Outline platelets.
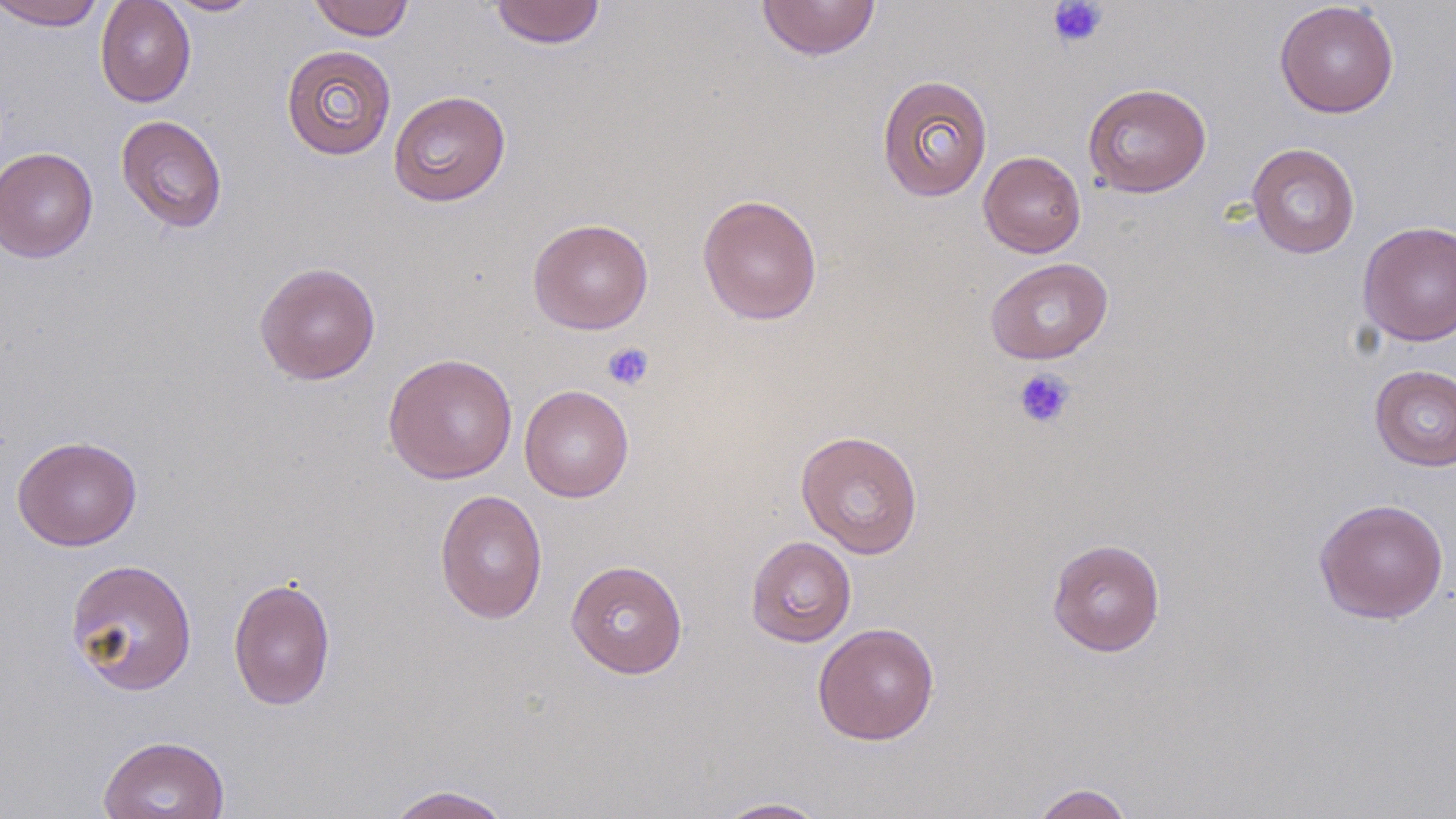
Approximate bounding boxes as named x1/y1/x2/y2 corners in pixels.
Platelets: (x1=1047, y1=0, x2=1109, y2=49), (x1=602, y1=341, x2=655, y2=391), (x1=1013, y1=368, x2=1076, y2=429).

Summary:
  - Uninfected red blood cell locations: (x1=1, y1=0, x2=106, y2=30), (x1=95, y1=0, x2=196, y2=107), (x1=161, y1=0, x2=266, y2=16), (x1=307, y1=0, x2=415, y2=41), (x1=489, y1=1, x2=606, y2=49), (x1=756, y1=1, x2=881, y2=60), (x1=1274, y1=1, x2=1399, y2=118), (x1=281, y1=45, x2=397, y2=160), (x1=876, y1=74, x2=993, y2=202), (x1=1083, y1=82, x2=1211, y2=198), (x1=388, y1=90, x2=511, y2=206), (x1=115, y1=114, x2=228, y2=233), (x1=1246, y1=142, x2=1360, y2=259), (x1=0, y1=146, x2=99, y2=263), (x1=978, y1=151, x2=1086, y2=257), (x1=697, y1=193, x2=823, y2=326), (x1=528, y1=218, x2=654, y2=334), (x1=1357, y1=220, x2=1456, y2=346), (x1=984, y1=257, x2=1114, y2=364), (x1=254, y1=261, x2=381, y2=385), (x1=383, y1=353, x2=518, y2=484), (x1=1370, y1=365, x2=1456, y2=471), (x1=519, y1=385, x2=634, y2=502), (x1=795, y1=429, x2=924, y2=559), (x1=12, y1=435, x2=142, y2=551), (x1=434, y1=489, x2=548, y2=623), (x1=1314, y1=497, x2=1449, y2=624), (x1=745, y1=535, x2=857, y2=648), (x1=1047, y1=538, x2=1165, y2=656), (x1=65, y1=558, x2=198, y2=695), (x1=566, y1=559, x2=688, y2=679), (x1=228, y1=576, x2=336, y2=711), (x1=812, y1=622, x2=939, y2=746), (x1=97, y1=734, x2=231, y2=819), (x1=1031, y1=783, x2=1135, y2=819), (x1=383, y1=784, x2=515, y2=819), (x1=712, y1=797, x2=831, y2=818)
  - Slide-level diagnosis: negative for blood parasites
  - Stain: May-Grünwald-Giemsa
  - Preparation: thin blood film
  - Modality: optical microscopy
  - Image size: 1456×819 pixels
  - Field of view: single
  - Magnification: 1000x